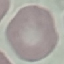

Result: no malaria parasites seen. Thin smear of blood. Giemsa stain. Automatically extracted cell patch, resized to 64 × 64 pixels. Photographed with a smartphone camera at the microscope eyepiece.